Assess this cell for malaria.
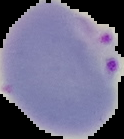
It is parasitized.

Summary:
  - Image type: cell region segmented out of the field of view; surrounding area masked to black
  - Image size: 124×139 pixels
  - Preparation: thin blood film